Locate every malaria parasite.
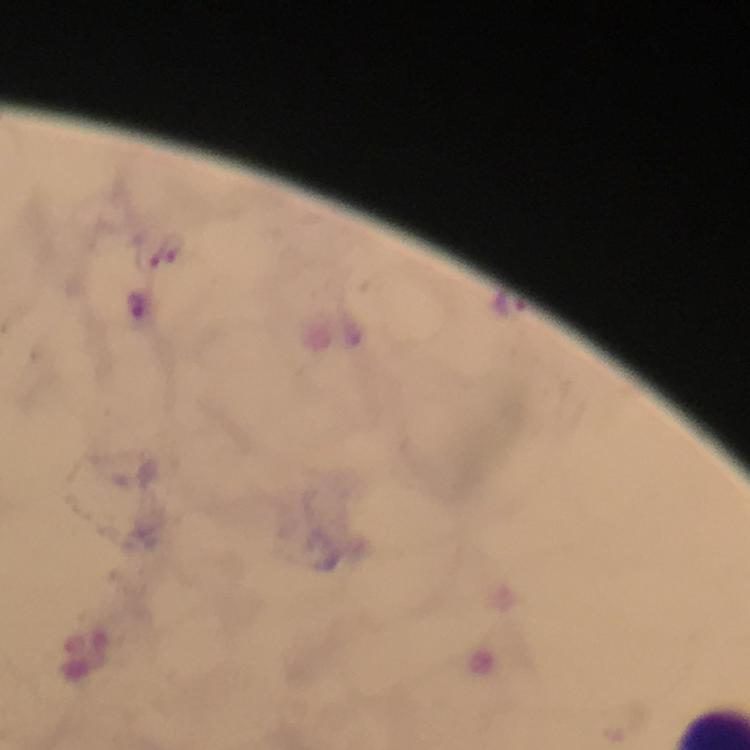
Approximate centers as {x, y} in pixels.
Malaria parasites: {510, 304}.

stain: Giemsa
capture: smartphone camera through the microscope
image_size: 750×750 pixels
magnification: 100x
cropped_from: one field of view
immersion_oil: applied
preparation: thick smear
context: from a diagnostic examination for malaria